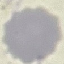
Summary:
  - Result: negative for malaria parasites
  - Image type: cell patch, automatically extracted from a larger field of view and resized to 64 × 64 pixels
  - Capture: smartphone through the microscope eyepiece
  - Stain: Giemsa
  - Preparation: thin blood film